Locate and identify every blood parasite.
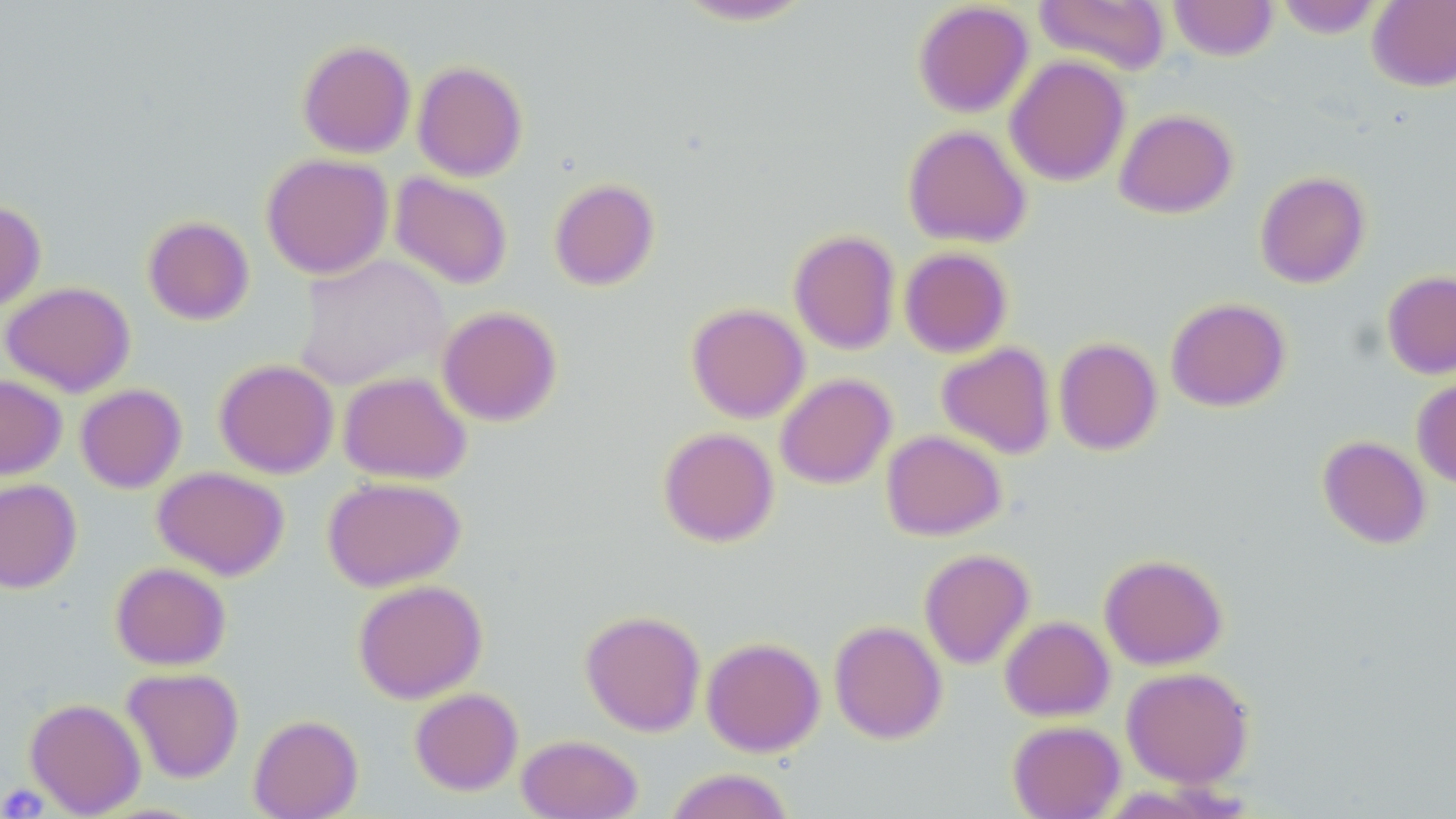

No blood parasites seen.

Summary:
  - Coordinate format: approximate bounding boxes as named x1/y1/x2/y2 corners in pixels
  - Platelet locations: (x1=0, y1=783, x2=50, y2=817)
  - Uninfected red blood cell locations: (x1=670, y1=0, x2=819, y2=27), (x1=1034, y1=0, x2=1170, y2=75), (x1=1168, y1=0, x2=1278, y2=61), (x1=1274, y1=0, x2=1383, y2=38), (x1=1367, y1=0, x2=1456, y2=92), (x1=913, y1=2, x2=1033, y2=118), (x1=297, y1=39, x2=416, y2=158), (x1=1005, y1=55, x2=1130, y2=186), (x1=412, y1=61, x2=527, y2=181), (x1=1114, y1=108, x2=1238, y2=218), (x1=902, y1=124, x2=1032, y2=248), (x1=261, y1=153, x2=393, y2=279), (x1=1255, y1=171, x2=1370, y2=288), (x1=390, y1=172, x2=513, y2=290), (x1=549, y1=177, x2=659, y2=290), (x1=0, y1=200, x2=46, y2=311), (x1=142, y1=215, x2=254, y2=325), (x1=788, y1=229, x2=900, y2=355), (x1=899, y1=247, x2=1013, y2=358), (x1=293, y1=254, x2=450, y2=390), (x1=1382, y1=270, x2=1456, y2=379), (x1=0, y1=281, x2=135, y2=397), (x1=1165, y1=297, x2=1290, y2=412), (x1=687, y1=302, x2=810, y2=423), (x1=437, y1=306, x2=562, y2=426), (x1=1053, y1=337, x2=1162, y2=455), (x1=936, y1=342, x2=1056, y2=459), (x1=214, y1=358, x2=339, y2=478), (x1=338, y1=371, x2=471, y2=484), (x1=775, y1=373, x2=896, y2=489), (x1=0, y1=374, x2=67, y2=479), (x1=1412, y1=376, x2=1456, y2=490), (x1=75, y1=384, x2=187, y2=493), (x1=658, y1=427, x2=779, y2=547), (x1=881, y1=430, x2=1006, y2=540), (x1=1318, y1=435, x2=1431, y2=549), (x1=152, y1=466, x2=289, y2=580), (x1=323, y1=475, x2=466, y2=592), (x1=0, y1=478, x2=81, y2=593), (x1=919, y1=549, x2=1035, y2=669), (x1=1099, y1=554, x2=1227, y2=670), (x1=110, y1=561, x2=231, y2=670), (x1=352, y1=579, x2=487, y2=703), (x1=580, y1=609, x2=706, y2=736), (x1=1000, y1=615, x2=1114, y2=722), (x1=829, y1=620, x2=947, y2=744), (x1=701, y1=636, x2=825, y2=757), (x1=1121, y1=666, x2=1254, y2=788), (x1=122, y1=667, x2=244, y2=783), (x1=409, y1=687, x2=523, y2=795), (x1=24, y1=697, x2=146, y2=817), (x1=248, y1=714, x2=363, y2=819), (x1=1007, y1=720, x2=1125, y2=819), (x1=516, y1=734, x2=643, y2=819), (x1=666, y1=767, x2=795, y2=819)
  - Slide-level diagnosis: negative for blood parasites
  - Field of view: single
  - Magnification: 1000x
  - Preparation: thin blood smear
  - Modality: light microscopy
  - Image size: 1456×819 pixels
  - Stain: May-Grünwald-Giemsa